Give the extent of all Plasmodium falciparum-infected red blood cells.
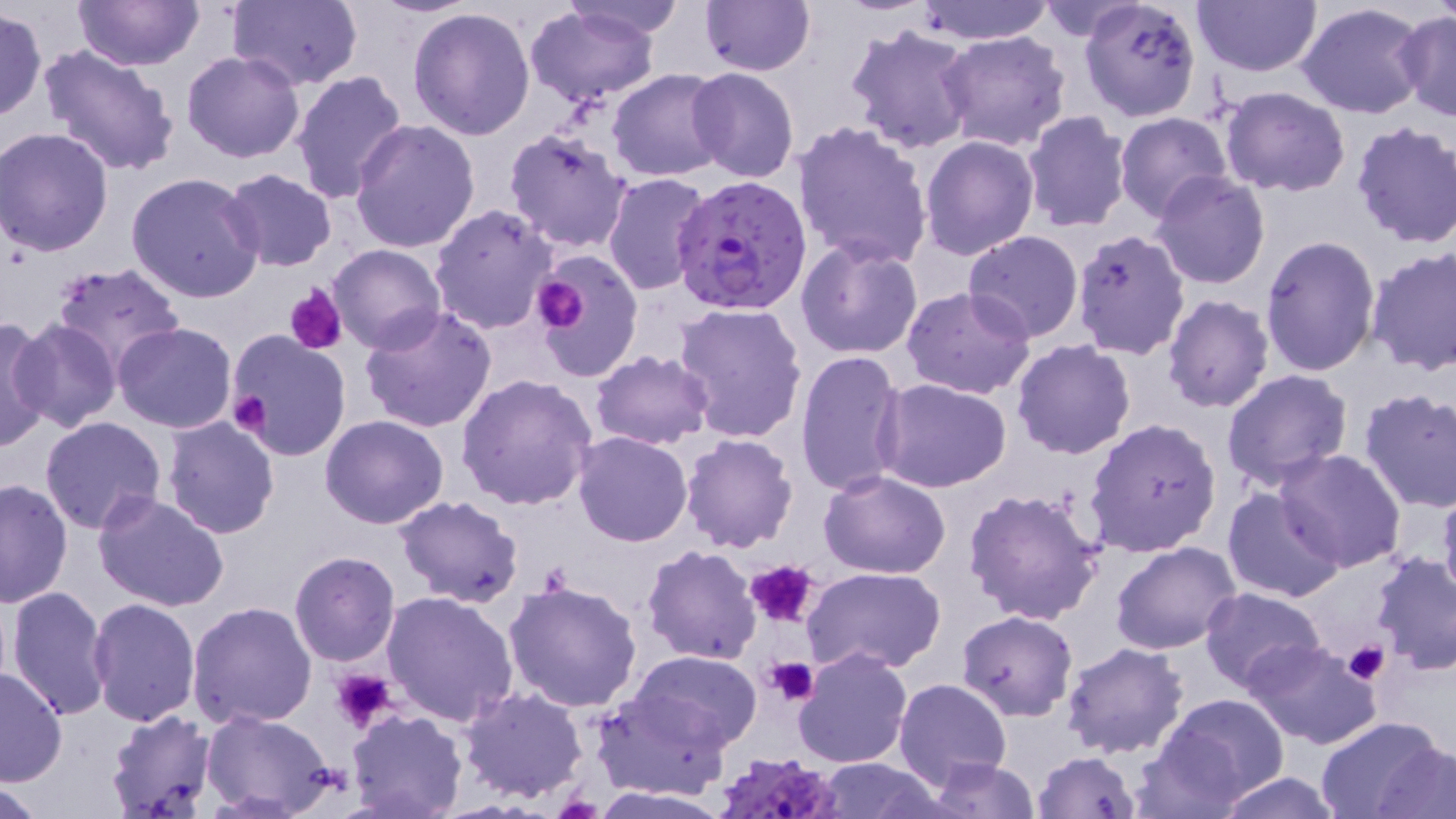

Approximate bounding boxes as [x1, y1, x2, y2] in pixels.
Plasmodium falciparum-infected red blood cells: [675, 175, 811, 314], [714, 747, 845, 819].

{
  "slide_level_diagnosis": "Plasmodium falciparum",
  "image_size": "1456×819 pixels",
  "stain": "May-Grünwald-Giemsa",
  "modality": "light microscopy",
  "preparation": "thin blood smear",
  "field_of_view": "single",
  "magnification": "1000x",
  "uninfected_red_blood_cell_locations": "approximate bounding boxes as [x1, y1, x2, y2] in pixels: [77, 0, 199, 71], [227, 0, 363, 89], [369, 0, 485, 17], [562, 0, 691, 40], [699, 0, 815, 77], [907, 0, 1057, 44], [1078, 0, 1203, 122], [1296, 0, 1432, 119], [1192, 1, 1325, 79], [524, 5, 660, 109], [407, 7, 537, 141], [0, 9, 47, 123], [1396, 11, 1456, 123], [845, 23, 977, 157], [939, 31, 1073, 152], [38, 42, 182, 177], [181, 50, 306, 163], [684, 68, 799, 183], [289, 70, 409, 204], [608, 70, 728, 181], [1220, 86, 1351, 198], [1021, 111, 1133, 234], [1114, 112, 1232, 223], [349, 118, 480, 252], [1350, 121, 1456, 249], [790, 122, 934, 271], [1, 126, 114, 256], [503, 127, 634, 253], [919, 135, 1040, 261], [220, 168, 338, 272], [603, 171, 714, 295], [125, 172, 265, 303], [1151, 172, 1271, 291], [429, 203, 559, 335], [1072, 230, 1190, 358], [963, 231, 1083, 343], [1260, 235, 1381, 376], [795, 238, 924, 359], [329, 243, 447, 353], [1366, 246, 1456, 375], [534, 251, 644, 381], [51, 264, 185, 379], [902, 285, 1036, 399], [1161, 293, 1276, 414], [670, 303, 808, 445], [357, 306, 498, 432], [0, 315, 54, 450], [10, 319, 123, 433], [114, 324, 237, 434], [225, 332, 352, 462], [1011, 340, 1136, 460], [588, 348, 714, 450], [795, 348, 908, 498], [1222, 370, 1353, 494], [456, 374, 598, 510], [874, 380, 1012, 494], [1358, 389, 1456, 514], [163, 415, 280, 538], [321, 415, 449, 530], [39, 416, 166, 535], [1083, 417, 1222, 557], [570, 432, 692, 547], [679, 433, 799, 554], [1273, 448, 1408, 572], [819, 470, 952, 580], [0, 477, 74, 609], [1437, 480, 1456, 611], [1223, 487, 1345, 603], [962, 488, 1106, 624], [93, 490, 230, 612], [394, 495, 524, 607], [1111, 541, 1242, 655], [642, 544, 761, 664], [289, 551, 400, 667], [1369, 552, 1456, 674], [802, 565, 947, 675], [502, 580, 643, 716], [6, 585, 113, 723], [1199, 585, 1327, 690], [380, 589, 518, 726], [85, 596, 200, 724], [186, 601, 317, 730], [956, 611, 1079, 721], [1243, 639, 1385, 750], [1060, 641, 1188, 760], [792, 647, 912, 768], [630, 651, 762, 748], [0, 664, 66, 788], [893, 678, 1012, 789], [457, 686, 588, 803], [592, 689, 734, 802], [1155, 693, 1289, 806], [104, 710, 217, 818], [346, 711, 468, 819], [203, 712, 338, 817], [1315, 715, 1449, 819], [1370, 734, 1454, 817], [1032, 749, 1142, 818], [926, 756, 1040, 817], [814, 758, 943, 818], [1214, 773, 1346, 818], [1, 780, 52, 818], [588, 787, 738, 819]",
  "platelet_locations": "approximate bounding boxes as [x1, y1, x2, y2] in pixels: [534, 277, 587, 332], [285, 285, 346, 354], [227, 391, 273, 437], [744, 558, 819, 629], [1345, 639, 1389, 685], [763, 655, 818, 706], [333, 667, 397, 731]"
}